Assess this cell for malaria.
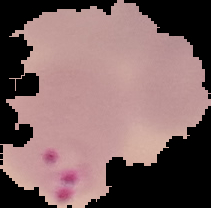
Parasitized.

Image is 211×208 pixels. Cell region segmented out of the field of view; the surrounding area is masked to black. From a thin blood smear.